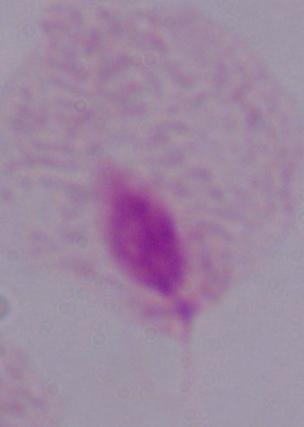
Summary:
  - Identification: trichomonad
  - Modality: micrograph
  - Magnification: 1000x